Report the malaria status of this cell.
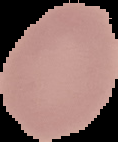
Uninfected.

Summary:
  - Image type: segmented cell region with the area outside set to black
  - Preparation: thin blood smear
  - Image size: 118×142 pixels